Report the malaria status of this cell.
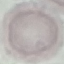

Uninfected.

Giemsa-stained preparation. Acquired by smartphone through the microscope eyepiece. Thin smear of blood. Automatically extracted cell patch, resized to 64 × 64 pixels.